Assess this cell for malaria.
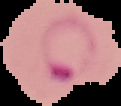

It is parasitized.

Summary:
  - Image type: segmented cell region on a black background
  - Image size: 121×106 pixels
  - Preparation: thin blood film